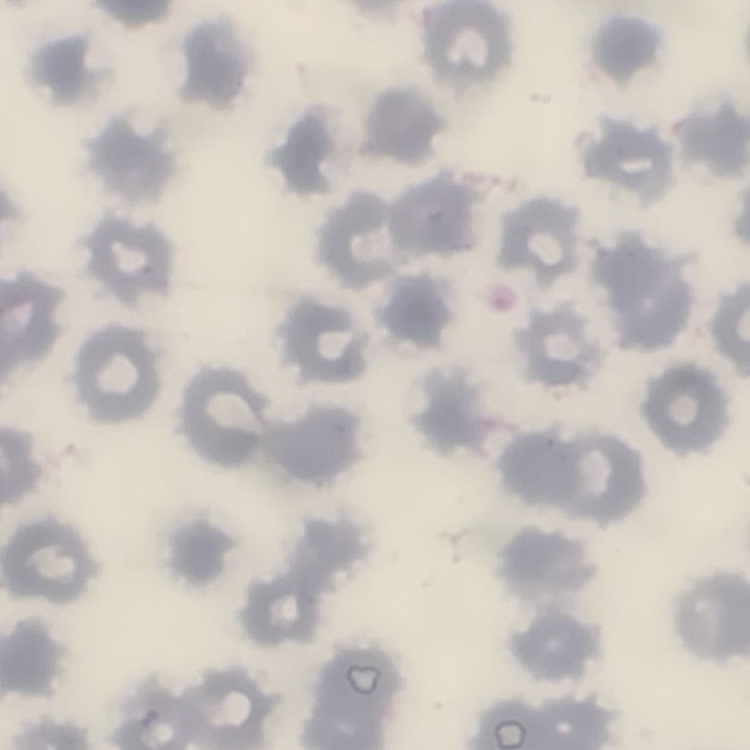

Summary:
  - Erythrocyte morphology: no rouleaux formation
  - Image type: square crop of a larger photomicrograph
  - Stain: Field's or Giemsa
  - Preparation: thin blood smear